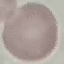

malaria status = uninfected
stain = Giemsa
capture = smartphone through the microscope eyepiece
image type = cell patch, automatically extracted from a larger field of view and resized to 64 × 64 pixels
preparation = thin smear